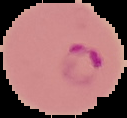

{
  "image_type": "segmented cell region with the area outside set to black",
  "image_size": "127×118 pixels",
  "preparation": "thin blood smear",
  "malaria_status": "parasitized"
}